Classify this cell by malaria status.
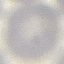

It is uninfected.

Photographed with a smartphone camera at the microscope eyepiece. Giemsa-stained preparation. Thin smear of blood. Automatically extracted cell patch, resized to 64 × 64 pixels.